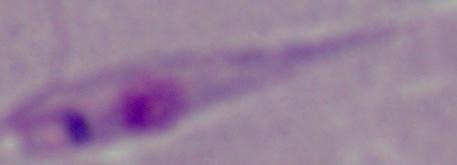

identification = Leishmania
magnification = 1000x
modality = photomicrograph